Name the blood parasite species.
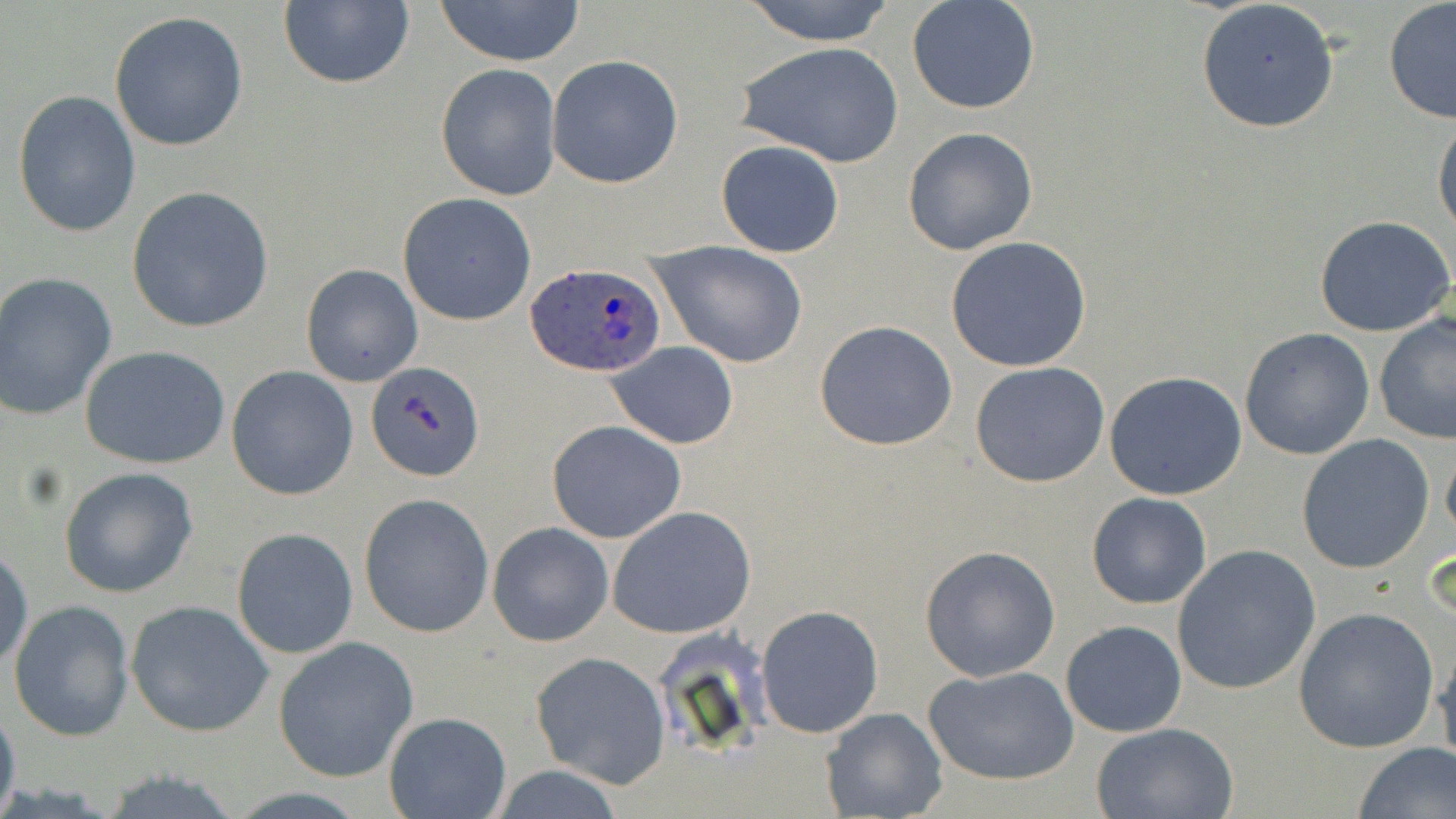
Plasmodium ovale.

Summary:
  - Coordinate format: approximate bounding boxes as (x1, y1, x2, y2) in pixels
  - Uninfected red blood cell locations: (432, 0, 588, 66), (740, 0, 898, 45), (277, 1, 415, 90), (1195, 1, 1340, 134), (906, 2, 1041, 115), (1382, 2, 1456, 124), (108, 10, 249, 152), (735, 40, 904, 168), (546, 55, 683, 187), (435, 65, 562, 201), (12, 88, 142, 238), (1433, 117, 1456, 243), (902, 126, 1039, 255), (716, 139, 845, 258), (126, 186, 274, 334), (396, 191, 537, 326), (1313, 215, 1456, 339), (946, 236, 1092, 371), (648, 240, 808, 367), (299, 262, 424, 388), (0, 271, 119, 420), (1373, 311, 1455, 448), (813, 319, 958, 451), (1239, 327, 1376, 462), (607, 342, 740, 450), (80, 344, 232, 470), (970, 361, 1111, 488), (367, 362, 485, 482), (226, 366, 360, 501), (1104, 370, 1248, 500), (546, 418, 686, 542), (1295, 434, 1434, 574), (1442, 443, 1456, 547), (60, 467, 198, 598), (1085, 492, 1212, 610), (358, 494, 494, 638), (607, 507, 755, 639), (488, 521, 614, 647), (232, 527, 359, 658), (0, 543, 33, 672), (1171, 544, 1321, 695), (919, 546, 1061, 681), (8, 599, 135, 742), (125, 600, 273, 737), (754, 605, 884, 739), (1294, 607, 1439, 753), (1060, 619, 1187, 738), (272, 636, 420, 783), (1435, 639, 1456, 771), (530, 652, 671, 790), (924, 666, 1080, 786), (0, 700, 20, 819), (822, 707, 947, 818), (384, 712, 510, 819), (1090, 722, 1239, 818), (1352, 742, 1456, 819)
  - Plasmodium ovale-infected red blood cell locations: (525, 263, 667, 378)
  - Magnification: 1000x
  - Preparation: thin blood film
  - Field of view: single
  - Stain: May-Grünwald-Giemsa
  - Modality: optical microscopy
  - Image size: 1456×819 pixels